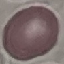
Summary:
  - Result: no malaria parasites detected
  - Image type: automatically extracted cell patch, resized to 64 × 64 pixels
  - Stain: Giemsa
  - Preparation: thin blood film
  - Capture: smartphone through the microscope eyepiece